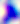

magnification = 400x
identification = Toxoplasma gondii
modality = photomicrograph